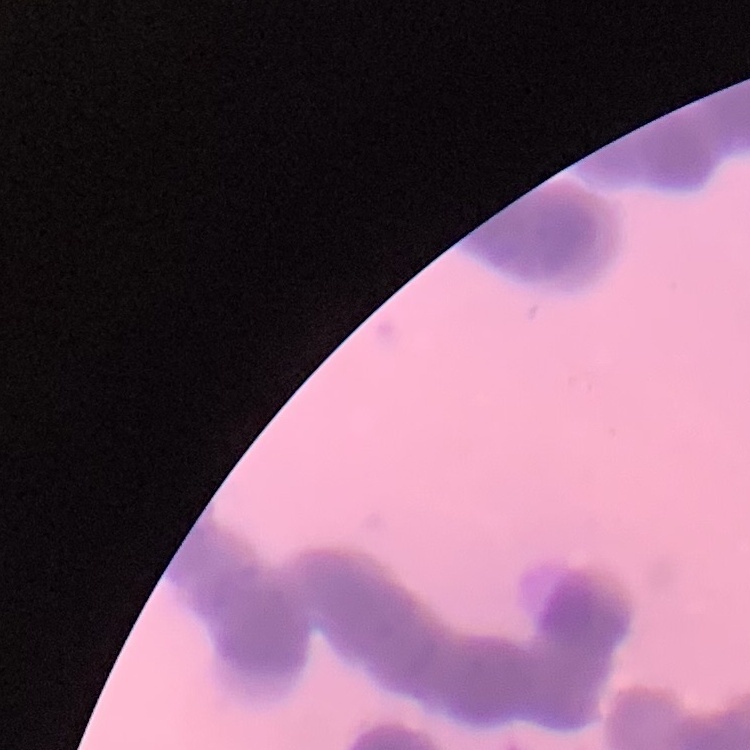 The erythrocytes exhibit rouleaux formation. Stained with either Field's or Giemsa. One tile cut from a larger photomicrograph. Thin blood film.